Assess the morphology of the erythrocytes.
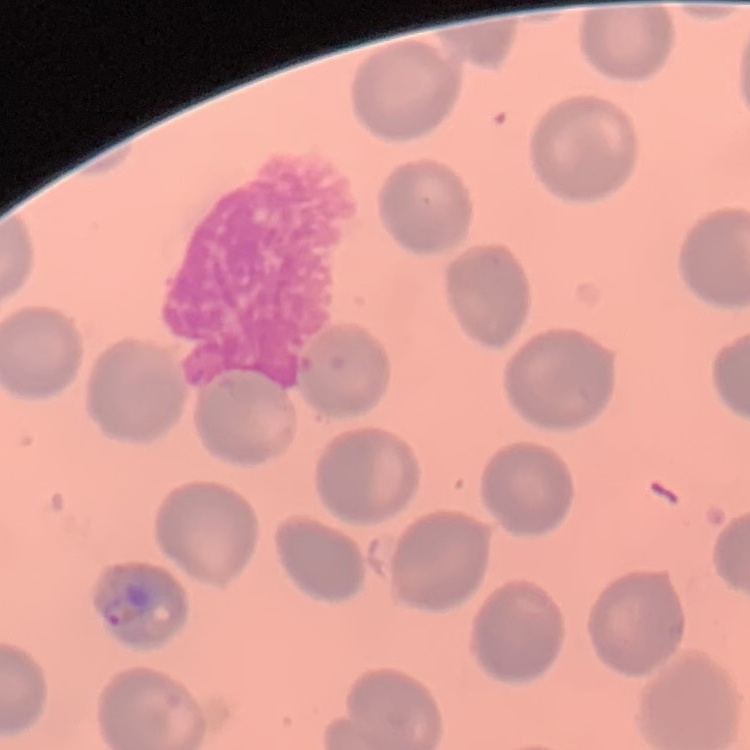

They show no rouleaux formation.

image_type: square crop of a larger photomicrograph
preparation: thin blood film
stain: Field's or Giemsa